Locate every Plasmodium vivax-infected red blood cell.
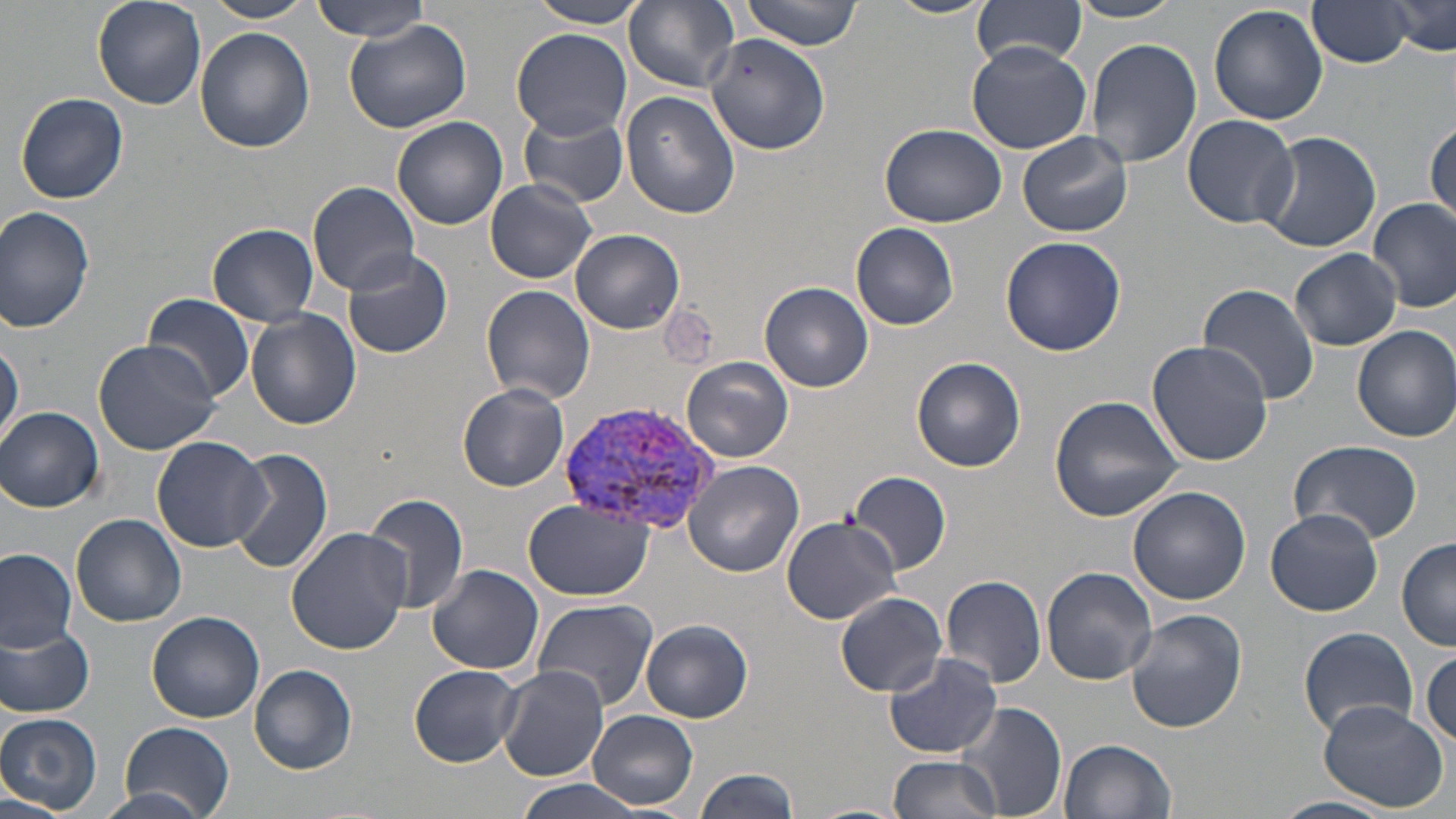

Approximate bounding boxes as (x1,y1)-(x2,y2) corner pairs in pixels.
Plasmodium vivax-infected red blood cells: (562,399)-(724,538).

Uninfected red blood cell locations: (91,0)-(207,111), (203,0)-(315,24), (311,0)-(429,44), (527,0)-(653,28), (883,0)-(995,19), (973,0)-(1089,68), (1305,0)-(1415,67), (1385,0)-(1454,58), (624,1)-(739,91), (739,1)-(865,50), (1065,1)-(1186,23), (1209,4)-(1329,126), (345,18)-(473,134), (194,26)-(315,154), (511,28)-(630,138), (707,34)-(831,155), (1084,38)-(1202,172), (966,40)-(1095,153), (16,91)-(128,204), (622,93)-(739,218), (519,110)-(630,207), (1182,113)-(1301,228), (391,116)-(510,229), (1426,117)-(1455,224), (880,123)-(1007,228), (1019,131)-(1134,237), (1255,131)-(1381,252), (485,178)-(596,283), (308,181)-(421,295), (1368,198)-(1456,312), (1,206)-(97,333), (851,222)-(959,330), (208,223)-(321,325), (571,228)-(686,333), (999,235)-(1128,355), (343,248)-(454,359), (1287,250)-(1403,351), (760,282)-(874,392), (1197,284)-(1320,405), (481,285)-(595,407), (142,293)-(255,402), (245,309)-(361,429), (1352,325)-(1456,442), (92,338)-(223,456), (1,340)-(23,447), (1145,340)-(1274,466), (912,356)-(1026,473), (682,357)-(793,462), (457,384)-(570,491), (1050,395)-(1184,521), (0,406)-(104,511), (151,436)-(268,550), (1288,439)-(1425,545), (226,446)-(333,577), (686,461)-(804,577), (847,470)-(951,576), (1127,485)-(1251,605), (363,494)-(469,616), (524,499)-(655,599), (1265,508)-(1383,616), (72,513)-(186,626), (780,514)-(903,624), (286,527)-(412,653), (1397,537)-(1456,649), (0,548)-(78,653), (426,564)-(545,675), (1040,567)-(1158,685), (940,573)-(1048,689), (835,592)-(947,696), (532,598)-(660,710), (1125,609)-(1247,733), (147,610)-(265,722), (641,620)-(754,722), (1,625)-(96,717), (1297,626)-(1420,738), (1420,648)-(1456,748), (883,653)-(1005,759), (249,664)-(357,774), (409,664)-(525,766), (497,667)-(611,782), (956,699)-(1068,819), (1318,702)-(1448,811), (587,709)-(699,809), (0,712)-(103,813), (119,721)-(235,817), (1060,737)-(1177,819), (889,754)-(1003,819), (693,767)-(798,819), (511,782)-(653,819), (94,789)-(215,819), (0,794)-(83,819), (1269,797)-(1394,819), (805,802)-(911,819). Slide-level diagnosis: Plasmodium vivax. Single field of view. May-Grünwald-Giemsa stain. Image is 1456×819 pixels. Captured at 1000x magnification. Thin blood film. Light microscopy.